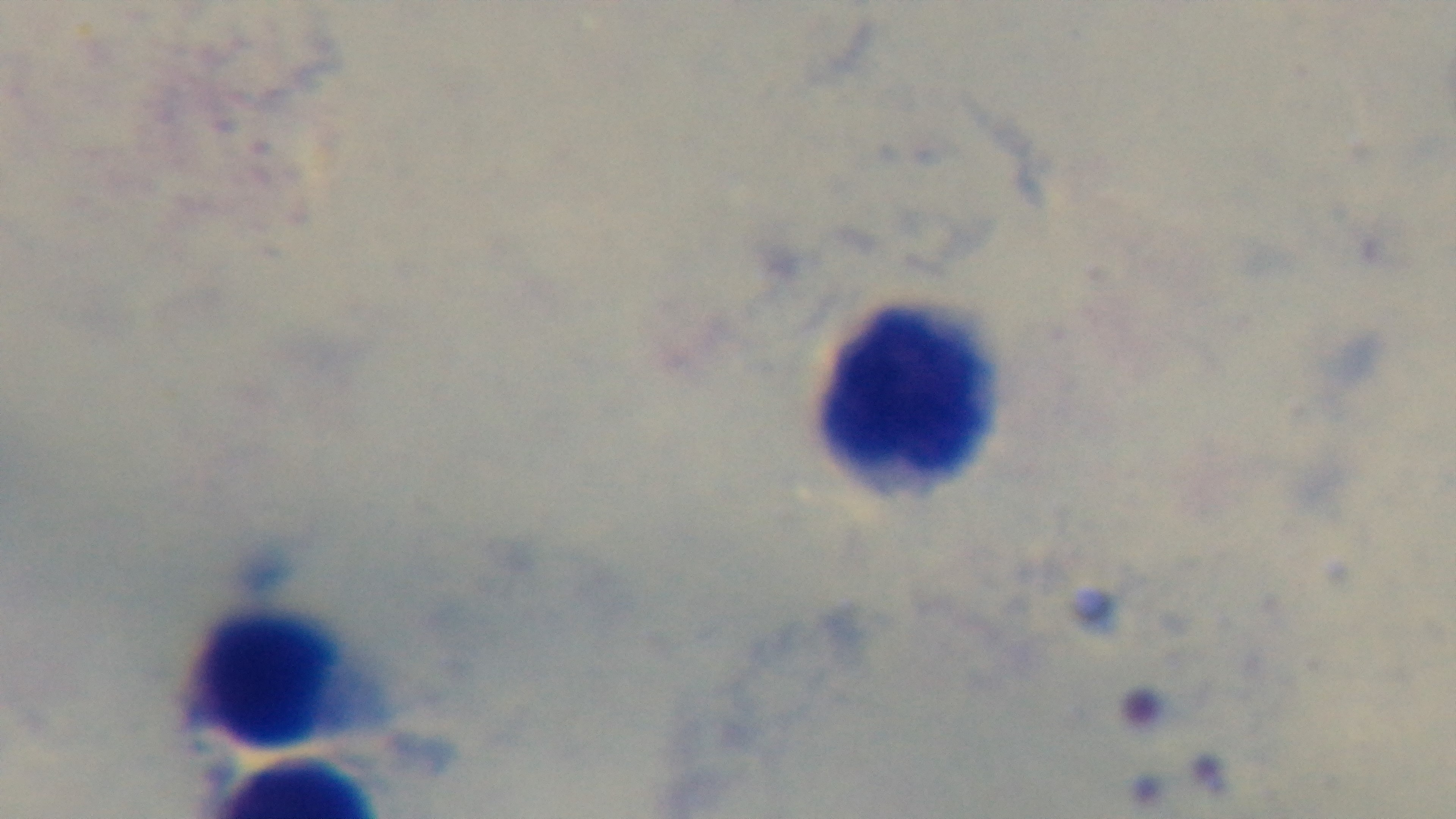

Summary:
  - Modality: light microscopy
  - Preparation: thick blood film
  - Field of view: single
  - Objective: 100x oil immersion
  - Stain: Giemsa
  - Malaria status: negative
  - Capture: mounted 4K digital camera